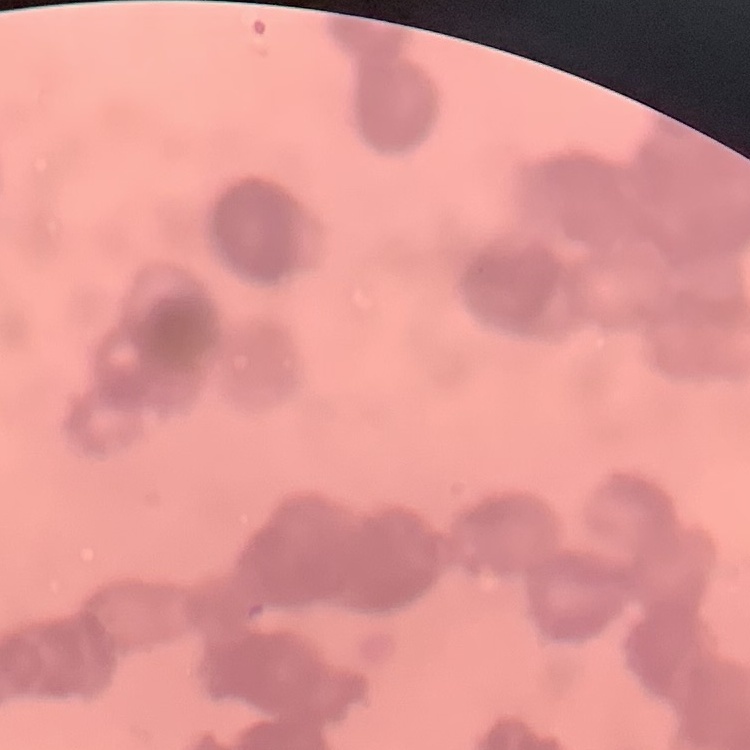

The red blood cells exhibit rouleaux formation. Thin blood smear. Stained with either Field's or Giemsa. One tile cut from a larger photomicrograph.